Report the malaria status of this cell.
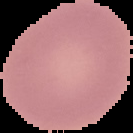

It is uninfected.

The area outside the segmented cell region is set to black. From a thin blood smear. Image is 133×133 pixels.